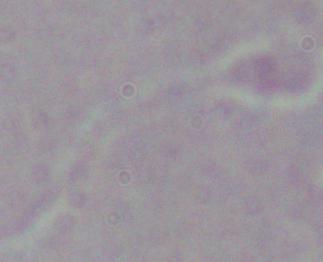

A Leishmania parasite is shown. Captured at 1000x magnification. Photomicrograph.